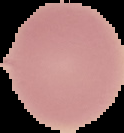

Summary:
  - Image size: 124×133 pixels
  - Malaria status: uninfected
  - Preparation: thin blood film
  - Image type: segmented cell region with the area outside set to black